Report the malaria status of this cell.
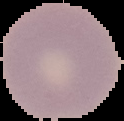

Uninfected.

From a thin blood film. The area outside the segmented cell region is set to black. Image is 124×121 pixels.